Name the parasite shown.
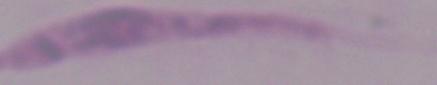
This is Leishmania.

Photomicrograph. Captured at 1000x magnification.